Comment on the morphology of the red blood cells.
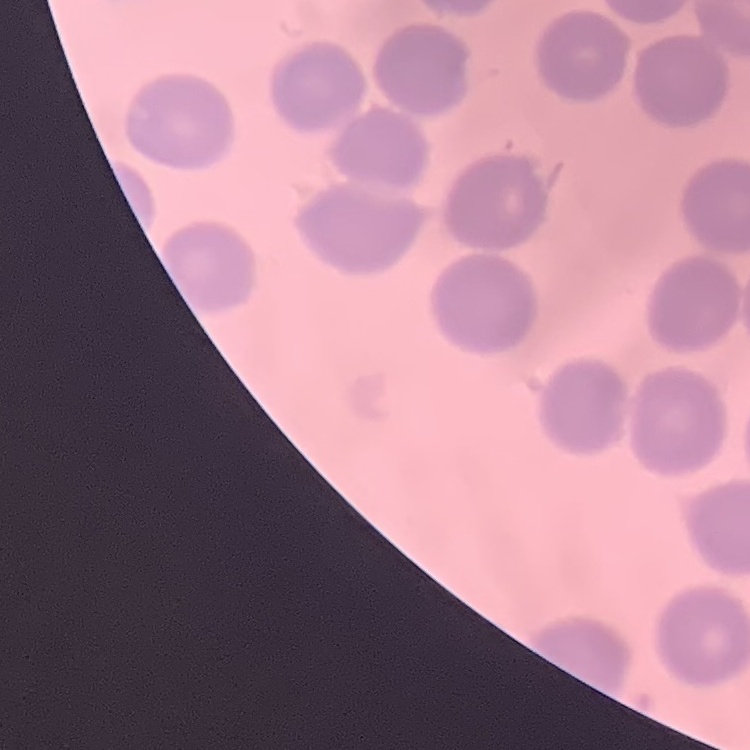
They show no rouleaux formation.

image type = one tile cut from a larger photomicrograph
stain = Field's or Giemsa
preparation = thin blood film